Locate every WBC.
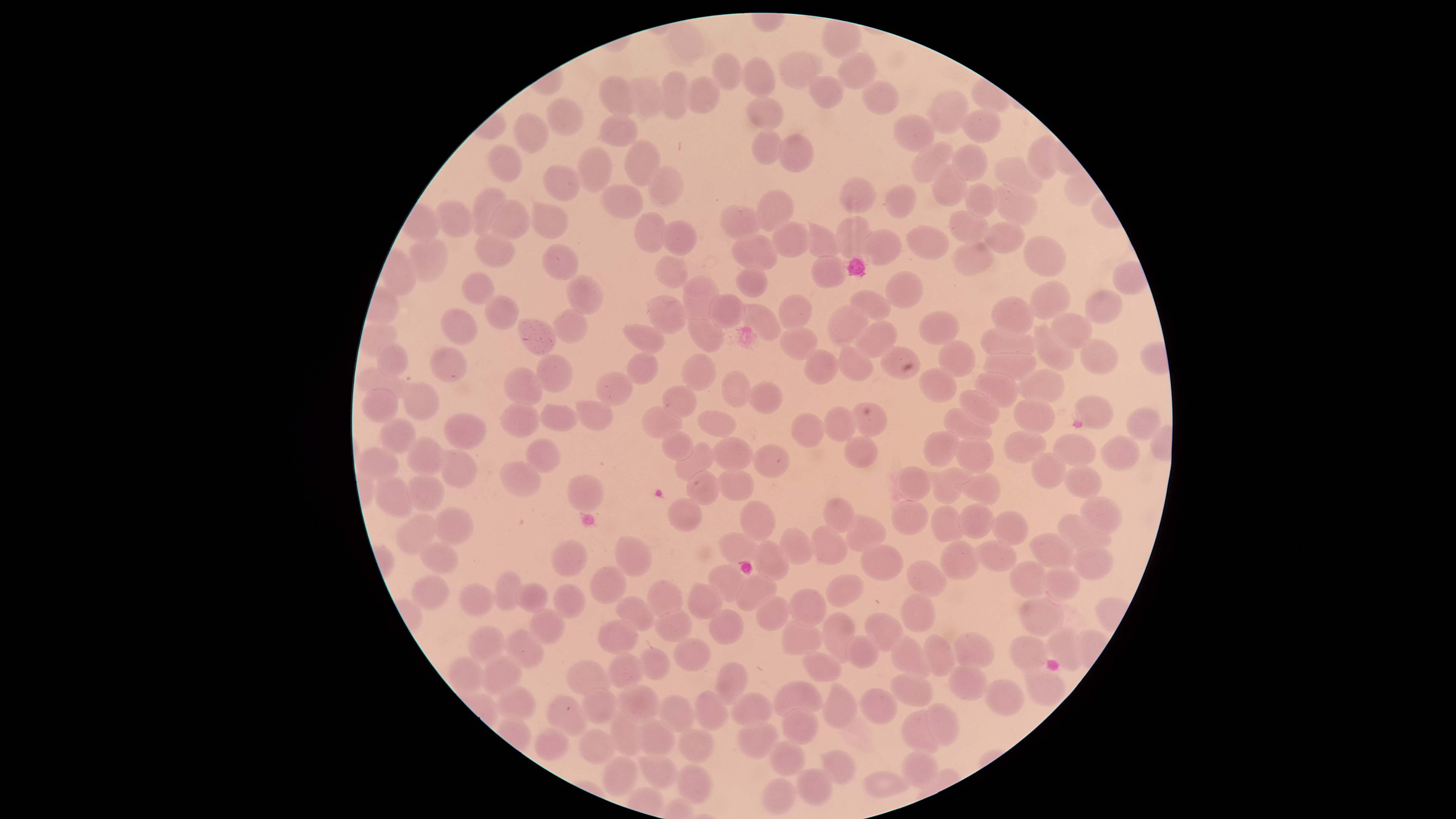

No WBCs identified.

Approximate bounding boxes as [left, top, right, bottom] in pixels.
Summary:
  - Uninfected RBCs: [823, 20, 861, 57], [779, 51, 816, 89], [712, 52, 742, 89], [838, 53, 875, 90], [742, 57, 776, 99], [660, 71, 688, 120], [600, 76, 637, 117], [682, 76, 721, 113], [808, 76, 843, 109], [622, 78, 665, 116], [863, 82, 899, 114], [928, 90, 969, 134], [746, 96, 785, 130], [547, 97, 583, 136], [959, 107, 1000, 142], [514, 113, 549, 153], [598, 115, 638, 146], [893, 115, 934, 151], [753, 130, 782, 165], [777, 134, 813, 172], [1027, 134, 1059, 180], [625, 140, 660, 187], [912, 142, 953, 182], [952, 144, 988, 181], [489, 145, 522, 182], [577, 147, 611, 192], [994, 156, 1045, 195], [933, 164, 968, 206], [543, 165, 581, 201], [647, 166, 683, 205], [839, 177, 877, 215], [965, 183, 999, 220], [993, 183, 1039, 225], [885, 184, 917, 219], [600, 186, 642, 219], [472, 187, 506, 234], [756, 189, 794, 232], [490, 199, 529, 238], [436, 200, 476, 237], [530, 203, 568, 239], [718, 205, 759, 242], [947, 209, 989, 245], [633, 212, 666, 254], [835, 216, 871, 259], [660, 220, 697, 254], [772, 221, 811, 257], [983, 222, 1026, 253], [805, 224, 840, 259], [906, 224, 950, 261], [860, 229, 902, 266], [731, 233, 778, 272], [475, 235, 514, 267], [408, 236, 448, 283], [1023, 236, 1066, 276], [952, 240, 996, 275], [541, 244, 579, 280], [655, 255, 688, 287], [811, 256, 847, 289], [736, 265, 767, 297], [885, 272, 922, 309], [461, 273, 495, 305], [565, 275, 604, 316], [681, 276, 720, 321], [1030, 280, 1069, 320], [850, 289, 892, 321], [1084, 289, 1122, 323], [709, 293, 745, 329], [779, 294, 811, 330], [484, 295, 520, 330], [649, 295, 686, 335], [991, 296, 1033, 337], [737, 304, 781, 340], [826, 304, 867, 345], [552, 308, 588, 344], [441, 309, 478, 347], [688, 311, 724, 353], [918, 311, 959, 345], [1052, 312, 1091, 349], [517, 318, 557, 355], [854, 321, 897, 358], [1034, 322, 1074, 370], [622, 324, 664, 354], [981, 325, 1037, 360], [780, 326, 818, 359], [1081, 338, 1119, 376], [938, 340, 976, 377], [377, 343, 408, 377], [838, 344, 873, 382], [880, 345, 921, 380], [984, 346, 1037, 381], [430, 347, 467, 383], [628, 351, 658, 385], [805, 351, 838, 384], [536, 354, 573, 393], [682, 354, 715, 392], [504, 367, 543, 405], [919, 367, 957, 403], [355, 369, 407, 400], [1017, 369, 1064, 403], [722, 371, 750, 408], [595, 372, 633, 407], [976, 372, 1019, 408], [747, 381, 783, 415], [402, 382, 439, 420], [663, 385, 697, 418], [361, 389, 399, 423], [960, 389, 1000, 426], [1075, 395, 1114, 430], [1013, 398, 1056, 434], [575, 400, 613, 431], [500, 401, 540, 439], [852, 402, 887, 438], [540, 404, 578, 431], [640, 406, 683, 439], [822, 407, 857, 442], [1128, 407, 1160, 441], [943, 408, 992, 443], [697, 410, 738, 437], [792, 412, 826, 447], [443, 413, 487, 450], [380, 418, 416, 456], [662, 430, 694, 461], [924, 430, 958, 467], [1004, 430, 1046, 464], [1054, 434, 1096, 466], [845, 435, 877, 468], [1102, 435, 1139, 470], [407, 436, 446, 476], [710, 436, 753, 472], [955, 437, 994, 474], [526, 439, 560, 473], [675, 443, 714, 480], [752, 444, 789, 479], [358, 448, 400, 481], [440, 450, 477, 488], [1031, 452, 1065, 489], [501, 461, 542, 496], [897, 465, 932, 500], [1064, 465, 1102, 497], [933, 467, 965, 504], [953, 467, 1001, 504], [716, 469, 755, 501], [687, 470, 720, 505], [374, 473, 414, 516], [406, 474, 445, 510], [568, 474, 604, 512], [1080, 496, 1123, 535], [668, 497, 703, 531], [823, 498, 856, 534], [891, 500, 928, 535], [741, 501, 774, 541], [958, 503, 995, 539], [931, 505, 964, 542], [433, 507, 474, 545], [991, 511, 1028, 546], [1057, 513, 1111, 552], [396, 514, 437, 554], [845, 514, 886, 552], [810, 525, 849, 564], [780, 528, 814, 566], [720, 532, 757, 564], [1029, 533, 1076, 570], [615, 535, 651, 577], [552, 539, 587, 577], [753, 539, 789, 580], [941, 540, 979, 581], [975, 540, 1017, 572], [419, 542, 459, 574], [861, 544, 904, 582], [1072, 545, 1114, 581], [907, 560, 948, 597], [1008, 561, 1051, 597], [709, 563, 747, 602], [1043, 565, 1080, 600], [591, 566, 626, 604], [494, 571, 521, 611], [735, 573, 777, 610], [826, 574, 864, 607], [413, 575, 449, 610], [646, 580, 683, 617], [458, 582, 495, 615], [516, 583, 547, 614], [687, 583, 723, 621], [555, 584, 584, 618], [790, 588, 827, 628], [899, 593, 936, 633], [757, 595, 789, 630], [616, 596, 655, 630], [1019, 599, 1063, 638], [529, 608, 565, 644], [655, 608, 693, 642], [709, 609, 744, 645], [822, 612, 854, 663], [865, 612, 903, 652], [597, 618, 639, 655], [782, 618, 822, 655], [468, 627, 506, 665], [504, 627, 544, 669], [1045, 627, 1085, 671], [954, 632, 995, 668], [845, 635, 879, 668], [891, 635, 930, 679], [922, 635, 954, 676], [1009, 637, 1048, 673], [674, 638, 710, 671], [640, 647, 671, 681], [607, 653, 644, 689], [800, 653, 842, 682], [448, 656, 484, 695], [481, 656, 522, 698], [566, 661, 611, 695], [716, 662, 749, 706], [948, 664, 988, 700], [1023, 667, 1066, 706], [890, 673, 933, 707], [984, 679, 1024, 715], [774, 681, 823, 717], [822, 681, 857, 728], [614, 684, 661, 722], [495, 685, 536, 720], [580, 687, 616, 724], [860, 688, 897, 725], [693, 691, 728, 731], [731, 693, 772, 725], [547, 694, 589, 736], [660, 696, 696, 733], [926, 703, 959, 746], [781, 708, 818, 745], [610, 709, 644, 755], [901, 710, 943, 754], [634, 719, 675, 756], [738, 720, 779, 759], [535, 728, 568, 760], [680, 728, 715, 763], [579, 729, 616, 764], [769, 741, 806, 776], [821, 750, 856, 784], [901, 750, 938, 789], [639, 753, 677, 790], [604, 757, 637, 796], [677, 765, 713, 804], [797, 769, 832, 805], [863, 772, 911, 799], [762, 778, 796, 814]
  - Preparation: thin blood film
  - Presence: no malaria parasites identified
  - Stain: Giemsa
  - Field of view: single
  - Capture: smartphone photograph through the microscope eyepiece
  - Image size: 1456×819 pixels
  - Visible region: circular